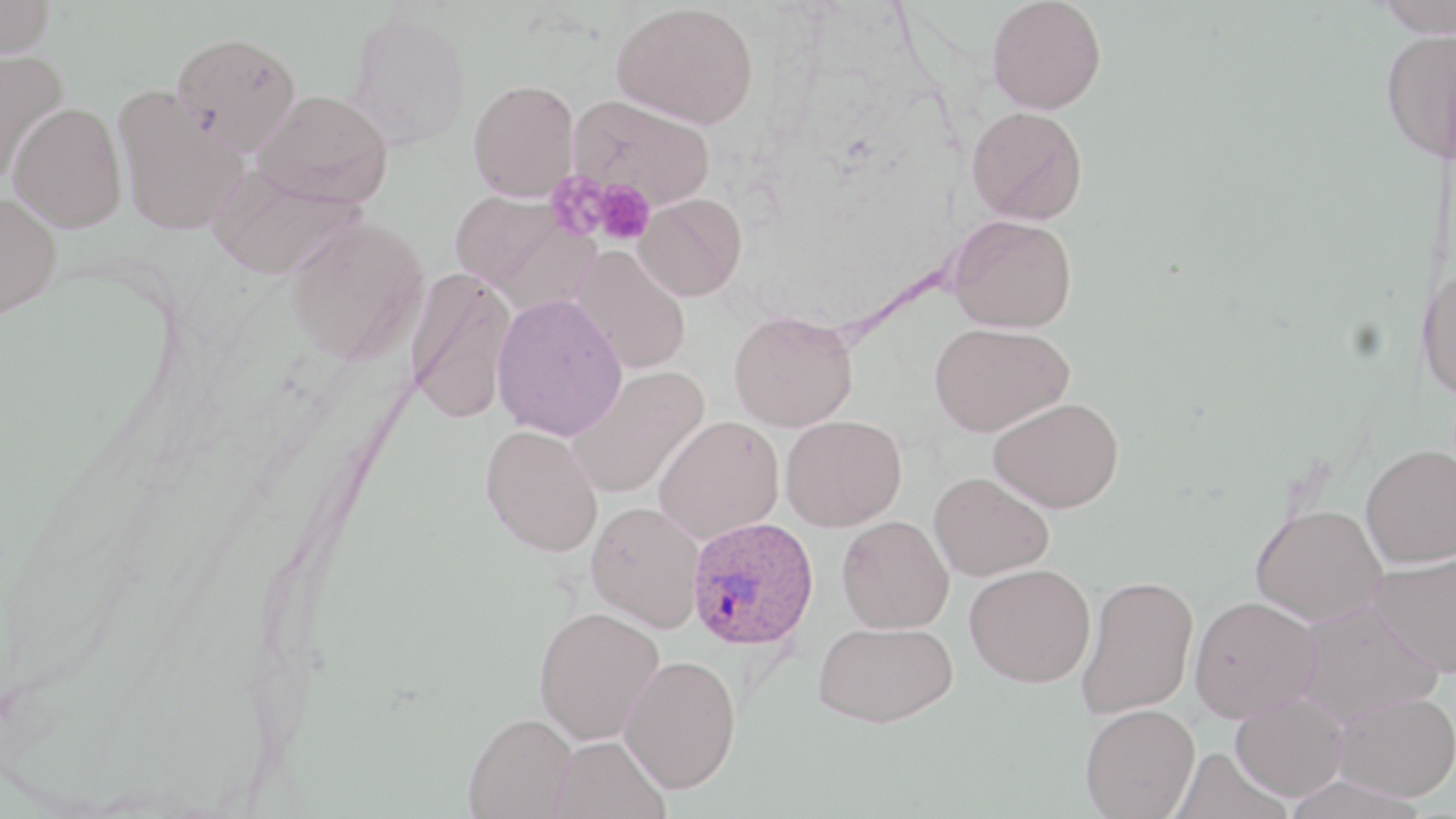

Summary:
  - Coordinate format: approximate bounding boxes as (x1, y1, x2, y2) in pixels
  - Plasmodium ovale-infected red blood cell locations: (686, 516, 820, 651)
  - Platelet locations: (546, 172, 610, 241), (593, 182, 655, 245)
  - Uninfected red blood cell locations: (0, 0, 55, 58), (987, 0, 1107, 115), (1374, 0, 1456, 37), (612, 2, 759, 128), (347, 10, 472, 151), (1380, 27, 1456, 164), (171, 31, 301, 154), (0, 50, 68, 180), (468, 79, 580, 201), (113, 86, 248, 236), (253, 89, 393, 207), (569, 94, 715, 211), (8, 102, 128, 232), (967, 106, 1088, 225), (207, 165, 364, 279), (449, 191, 593, 308), (0, 192, 61, 320), (634, 193, 747, 301), (949, 214, 1077, 332), (286, 216, 429, 364), (572, 246, 691, 375), (1416, 265, 1456, 399), (405, 268, 517, 424), (491, 293, 628, 441), (729, 311, 858, 432), (929, 322, 1074, 436), (566, 366, 709, 499), (989, 397, 1124, 513), (781, 415, 907, 532), (653, 417, 784, 545), (480, 424, 603, 557), (1360, 444, 1456, 569), (928, 471, 1054, 581), (586, 501, 705, 632), (1251, 504, 1387, 625), (837, 515, 954, 634), (1368, 553, 1456, 677), (965, 563, 1096, 687), (1077, 574, 1199, 718), (1189, 596, 1321, 722), (1294, 599, 1443, 726), (533, 606, 665, 745), (813, 620, 958, 727), (619, 654, 741, 793), (1331, 691, 1456, 802), (1231, 693, 1348, 802), (1080, 703, 1199, 819), (463, 713, 577, 818), (548, 735, 670, 819)
  - Slide-level diagnosis: Plasmodium ovale
  - Image size: 1456×819 pixels
  - Preparation: thin blood film
  - Magnification: 1000x
  - Field of view: one of a larger specimen
  - Stain: May-Grünwald-Giemsa
  - Modality: optical microscopy